Assess this cell for malaria.
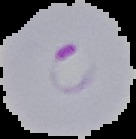
It is parasitized.

preparation = thin blood film
image size = 136×139 pixels
image type = segmented cell region with the area outside set to black